State which cell type is depicted.
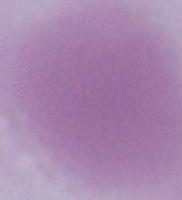

This is an erythrocyte.

magnification = 1000x
modality = photomicrograph